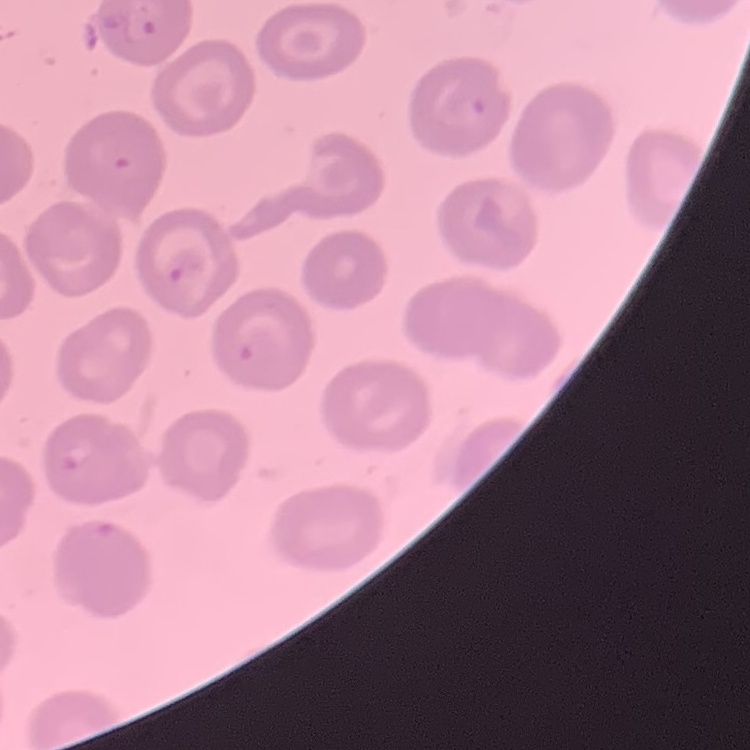
The erythrocytes exhibit no rouleaux formation. Field's or Giemsa stain. One tile cut from a larger photomicrograph. Thin blood smear.